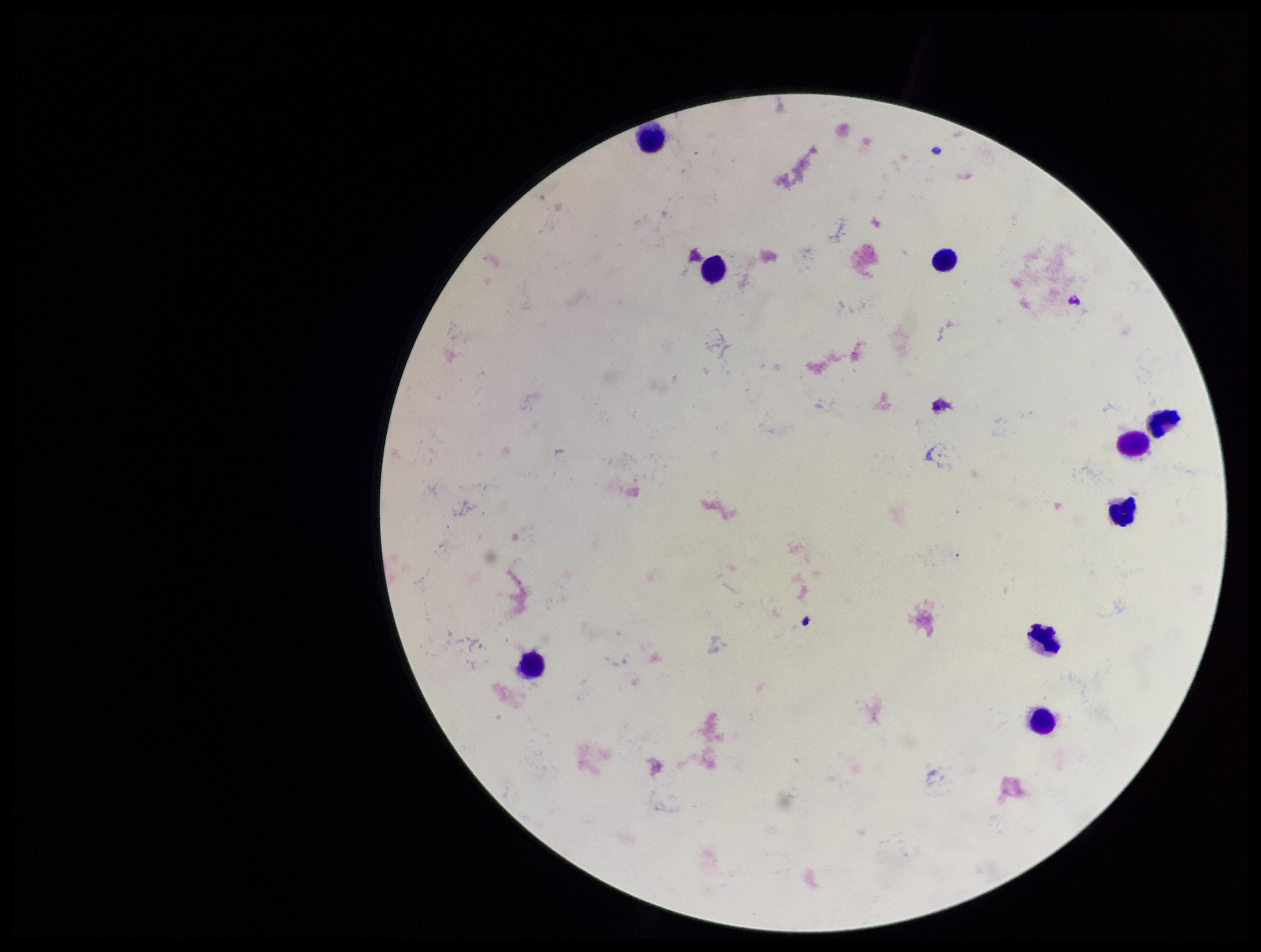 Preparation: thick. Leukocyte count: 9. Plasmodium parasites: none identified. Image is 1261×952 pixels. Parasite count: 0. Photographed through the microscope eyepiece with a smartphone camera. Single field of view. Patient malaria status: negative. Giemsa stain.